Report the malaria status of this cell.
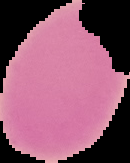

Uninfected.

Summary:
  - Image type: cell region segmented out of the field of view; surrounding area masked to black
  - Preparation: thin blood smear
  - Image size: 130×163 pixels